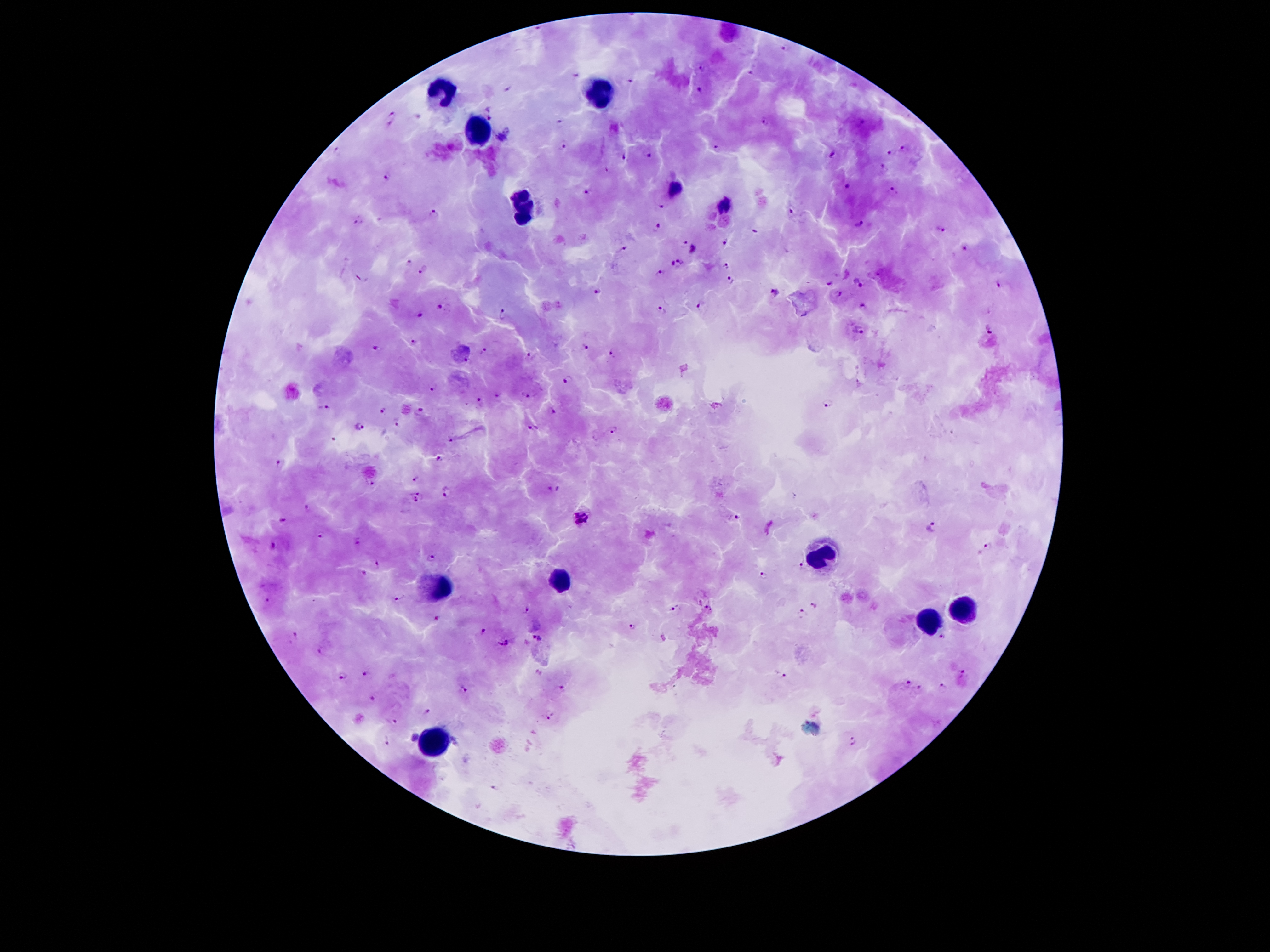 Approximate object centers, in pixels from the top-left corner. Leukocyte locations: (x=441, y=91), (x=597, y=93), (x=480, y=134), (x=521, y=206), (x=825, y=554), (x=561, y=578), (x=442, y=589), (x=962, y=607), (x=926, y=621), (x=430, y=741). Plasmodium parasite locations: (x=705, y=70), (x=753, y=71), (x=576, y=73), (x=629, y=79), (x=507, y=87), (x=700, y=91), (x=488, y=108), (x=417, y=114), (x=490, y=117), (x=392, y=118), (x=557, y=123), (x=765, y=123), (x=504, y=137), (x=563, y=147), (x=716, y=147), (x=902, y=148), (x=890, y=151), (x=833, y=154), (x=650, y=155), (x=623, y=156), (x=882, y=166), (x=391, y=175), (x=848, y=184), (x=676, y=187), (x=893, y=191), (x=588, y=193), (x=725, y=205), (x=663, y=206), (x=792, y=210), (x=434, y=214), (x=359, y=222), (x=858, y=223), (x=657, y=228), (x=941, y=228), (x=757, y=232), (x=685, y=242), (x=725, y=242), (x=624, y=249), (x=695, y=249), (x=964, y=249), (x=681, y=259), (x=409, y=262), (x=729, y=265), (x=675, y=266), (x=423, y=268), (x=661, y=274), (x=361, y=277), (x=729, y=279), (x=860, y=282), (x=831, y=283), (x=597, y=291), (x=774, y=293), (x=840, y=293), (x=703, y=303), (x=443, y=307), (x=864, y=307), (x=663, y=309), (x=423, y=315), (x=504, y=316), (x=989, y=328), (x=857, y=331), (x=413, y=341), (x=586, y=345), (x=375, y=348), (x=482, y=351), (x=614, y=352), (x=532, y=356), (x=566, y=379), (x=432, y=388), (x=497, y=395), (x=528, y=395), (x=479, y=402), (x=828, y=403), (x=322, y=408), (x=383, y=409), (x=554, y=411), (x=420, y=412), (x=396, y=422), (x=360, y=426), (x=532, y=427), (x=613, y=428), (x=333, y=438), (x=451, y=438), (x=438, y=459), (x=279, y=464), (x=417, y=477), (x=370, y=483), (x=553, y=489), (x=445, y=492), (x=418, y=496), (x=309, y=509), (x=581, y=516), (x=737, y=518), (x=282, y=519), (x=932, y=527), (x=319, y=532), (x=358, y=540), (x=271, y=544), (x=989, y=546), (x=431, y=555), (x=377, y=562), (x=801, y=565), (x=364, y=571), (x=764, y=577), (x=266, y=598), (x=401, y=598), (x=813, y=605), (x=527, y=607), (x=673, y=607), (x=708, y=609), (x=797, y=614), (x=438, y=618), (x=631, y=626), (x=484, y=631), (x=295, y=635), (x=942, y=636), (x=538, y=638), (x=504, y=641), (x=366, y=671), (x=963, y=673), (x=780, y=674), (x=345, y=675), (x=908, y=683), (x=942, y=686), (x=920, y=688), (x=464, y=689), (x=563, y=689), (x=371, y=697), (x=427, y=712), (x=552, y=715), (x=390, y=721), (x=414, y=738), (x=387, y=740), (x=853, y=741), (x=494, y=786). Single field of view. 100x magnification. Thick blood smear. Patient malaria status: infected with Plasmodium falciparum. Giemsa-stained preparation. Image is 1270×952 pixels. Smartphone photograph taken through the microscope eyepiece.